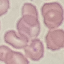
Result: negative for malaria parasites. Acquired by smartphone through the microscope eyepiece. Automatically extracted cell patch, resized to 64 × 64 pixels. Giemsa-stained preparation. Thin blood smear.